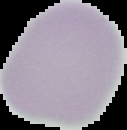
malaria_status: uninfected
preparation: thin blood film
image_size: 127×130 pixels
image_type: cell region segmented out of the field of view; surrounding area masked to black